Report the malaria status of this cell.
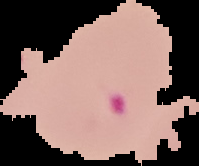

Parasitized.

Image is 199×166 pixels. From a thin blood film. Cell region segmented out of the field of view; the surrounding area is masked to black.